Locate and identify every blood parasite.
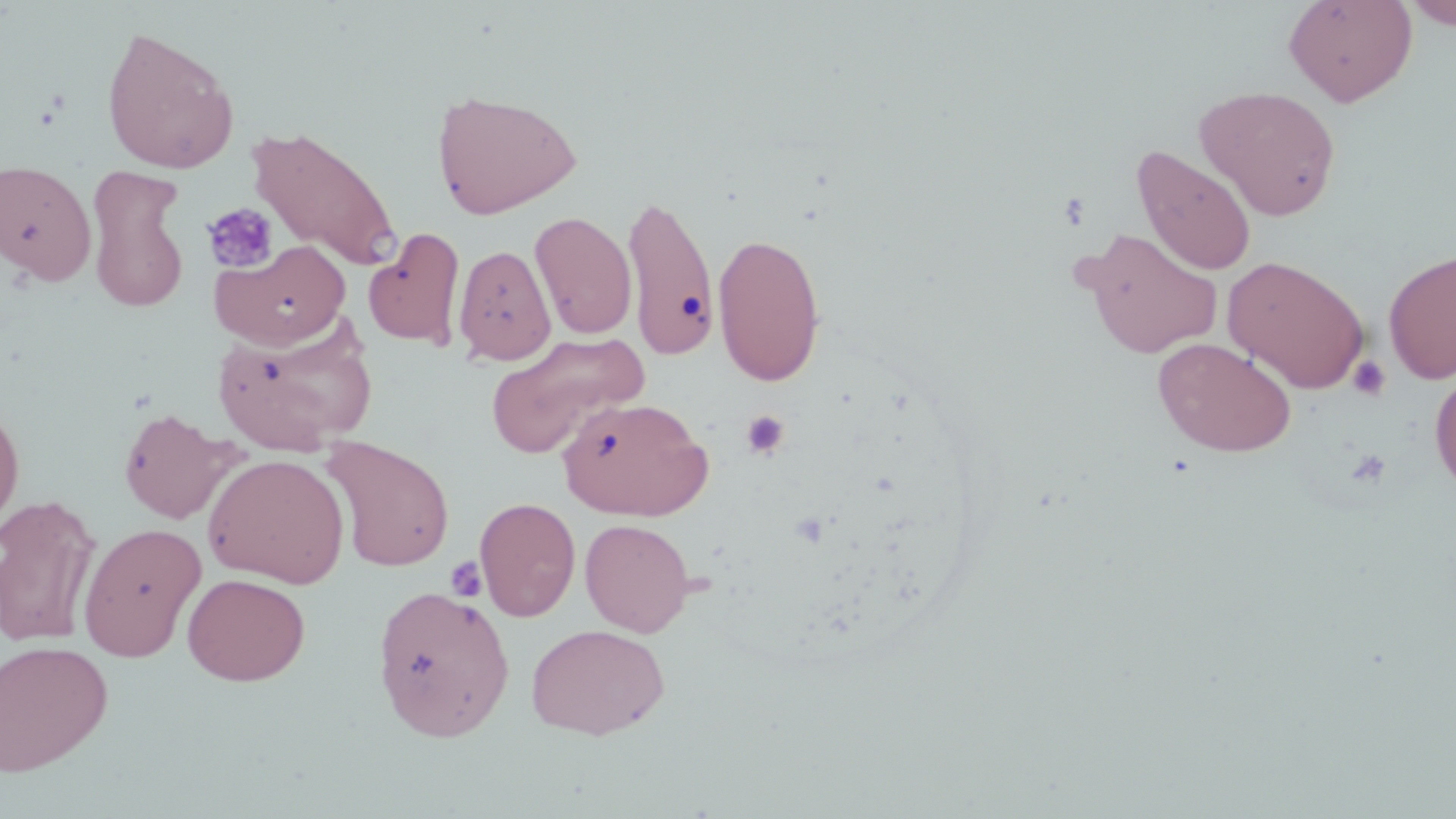

No blood parasites observed.

{
  "slide_level_diagnosis": "no evidence of blood parasites",
  "magnification": "1000x",
  "image_size": "1456×819 pixels",
  "field_of_view": "one of a larger specimen",
  "preparation": "thin blood film",
  "uninfected_red_blood_cell_locations": "approximate bounding boxes as (x1, y1, x2, y2) in pixels: (1283, 0, 1418, 107), (1402, 1, 1456, 30), (100, 24, 240, 174), (1194, 85, 1342, 221), (431, 88, 582, 220), (246, 124, 402, 271), (1132, 145, 1257, 276), (0, 159, 97, 286), (85, 166, 191, 314), (622, 192, 720, 362), (529, 211, 637, 340), (363, 227, 466, 350), (1078, 227, 1223, 359), (712, 231, 826, 387), (212, 239, 351, 349), (453, 244, 556, 365), (1383, 249, 1456, 384), (1222, 255, 1370, 393), (214, 319, 376, 454), (485, 331, 648, 459), (1153, 338, 1296, 457), (1430, 369, 1456, 495), (558, 396, 713, 520), (0, 400, 25, 535), (118, 407, 240, 524), (320, 435, 456, 572), (202, 453, 350, 588), (0, 495, 102, 648), (474, 497, 580, 622), (580, 518, 696, 637), (78, 522, 207, 662), (182, 572, 310, 685), (372, 584, 514, 742), (526, 623, 671, 740), (0, 640, 114, 776)",
  "stain": "May-Grünwald-Giemsa",
  "modality": "light microscopy",
  "platelet_locations": "approximate bounding boxes as (x1, y1, x2, y2) in pixels: (201, 202, 279, 274), (1347, 356, 1391, 402), (740, 410, 790, 460), (1347, 450, 1390, 488), (445, 556, 487, 602)"
}